Classify this cell by malaria status.
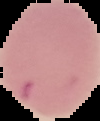

It is parasitized.

image type = segmented cell region on a black background
image size = 100×121 pixels
preparation = thin blood film